Outline each blood parasite and name the species.
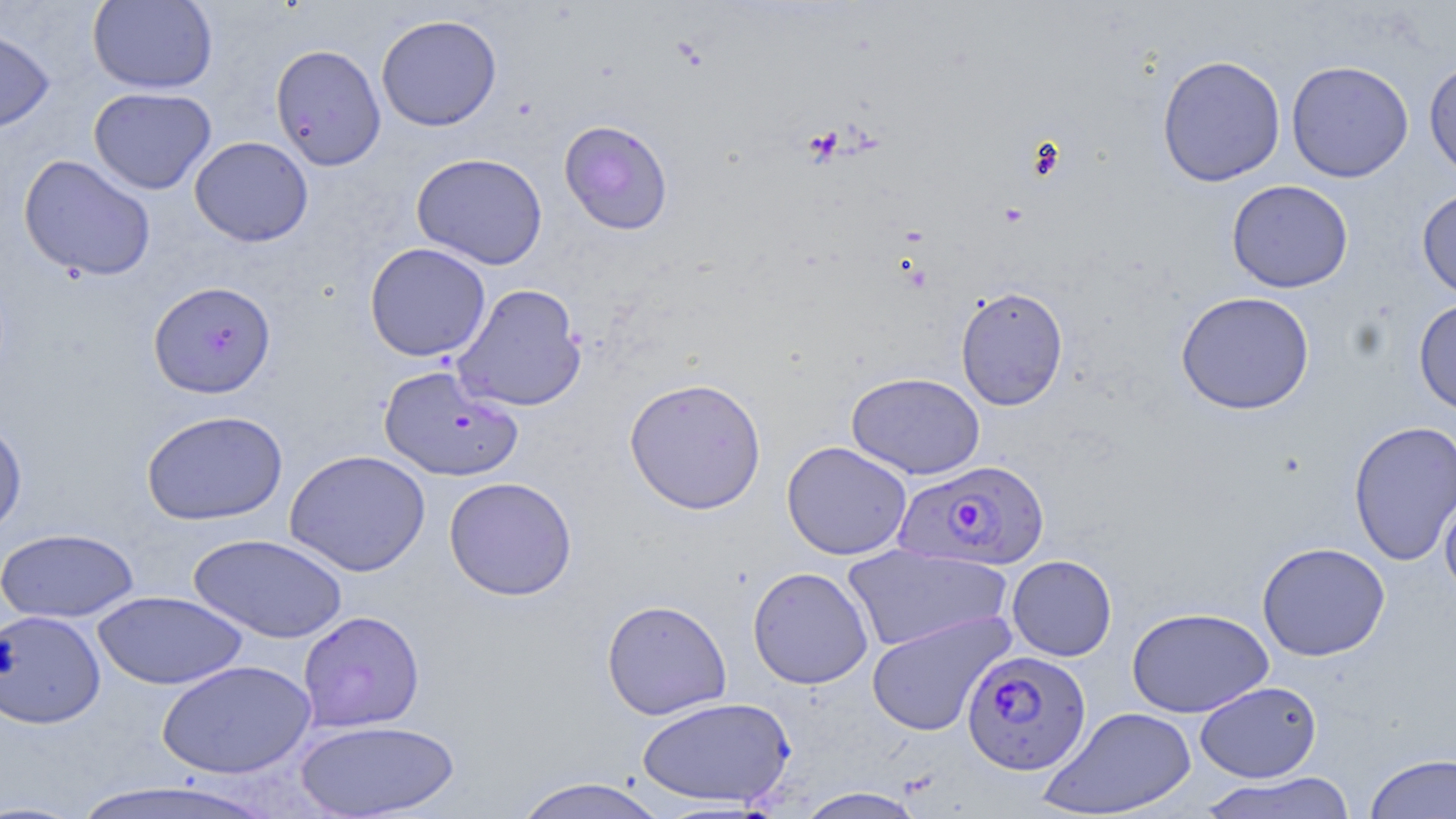
Approximate bounding boxes as (x1, y1, x2, y2) in pixels.
Plasmodium falciparum-infected red blood cells: (893, 459, 1050, 572), (961, 650, 1092, 775).
No Plasmodium ovale, Plasmodium malariae, Plasmodium vivax, Babesia divergens, or Trypanosoma brucei observed.

Summary:
  - Uninfected red blood cell locations: (87, 0, 218, 94), (375, 13, 502, 132), (0, 25, 54, 134), (269, 43, 386, 170), (1157, 54, 1286, 187), (1423, 59, 1456, 183), (1286, 60, 1414, 182), (88, 86, 217, 195), (558, 119, 674, 235), (189, 136, 313, 247), (411, 153, 548, 269), (18, 154, 156, 282), (1226, 179, 1353, 293), (1416, 186, 1456, 301), (364, 242, 491, 362), (148, 281, 277, 398), (452, 283, 587, 412), (955, 286, 1069, 411), (1175, 291, 1315, 415), (1413, 297, 1456, 416), (378, 364, 523, 482), (846, 372, 985, 479), (624, 376, 767, 514), (140, 409, 288, 525), (0, 417, 28, 538), (1348, 420, 1456, 566), (782, 441, 912, 560), (284, 449, 431, 577), (444, 476, 577, 601), (1440, 491, 1456, 602), (0, 527, 140, 623), (188, 533, 348, 643), (1257, 542, 1390, 661), (842, 544, 1011, 653), (1006, 555, 1117, 661), (747, 566, 873, 689), (93, 591, 247, 689), (601, 599, 732, 720), (1127, 607, 1273, 719), (0, 610, 107, 730), (297, 610, 425, 732), (866, 611, 1013, 736), (157, 659, 316, 779), (1195, 681, 1322, 783), (636, 696, 795, 809), (1040, 706, 1198, 818), (294, 719, 460, 819), (1364, 752, 1456, 818), (1198, 771, 1358, 818), (510, 776, 670, 819), (68, 778, 282, 819), (794, 787, 927, 818)
  - Slide-level diagnosis: Plasmodium falciparum
  - Modality: light microscopy
  - Field of view: one of a larger specimen
  - Stain: May-Grünwald-Giemsa
  - Magnification: 1000x
  - Preparation: thin blood smear
  - Image size: 1456×819 pixels